Locate every Plasmodium vivax-infected red blood cell.
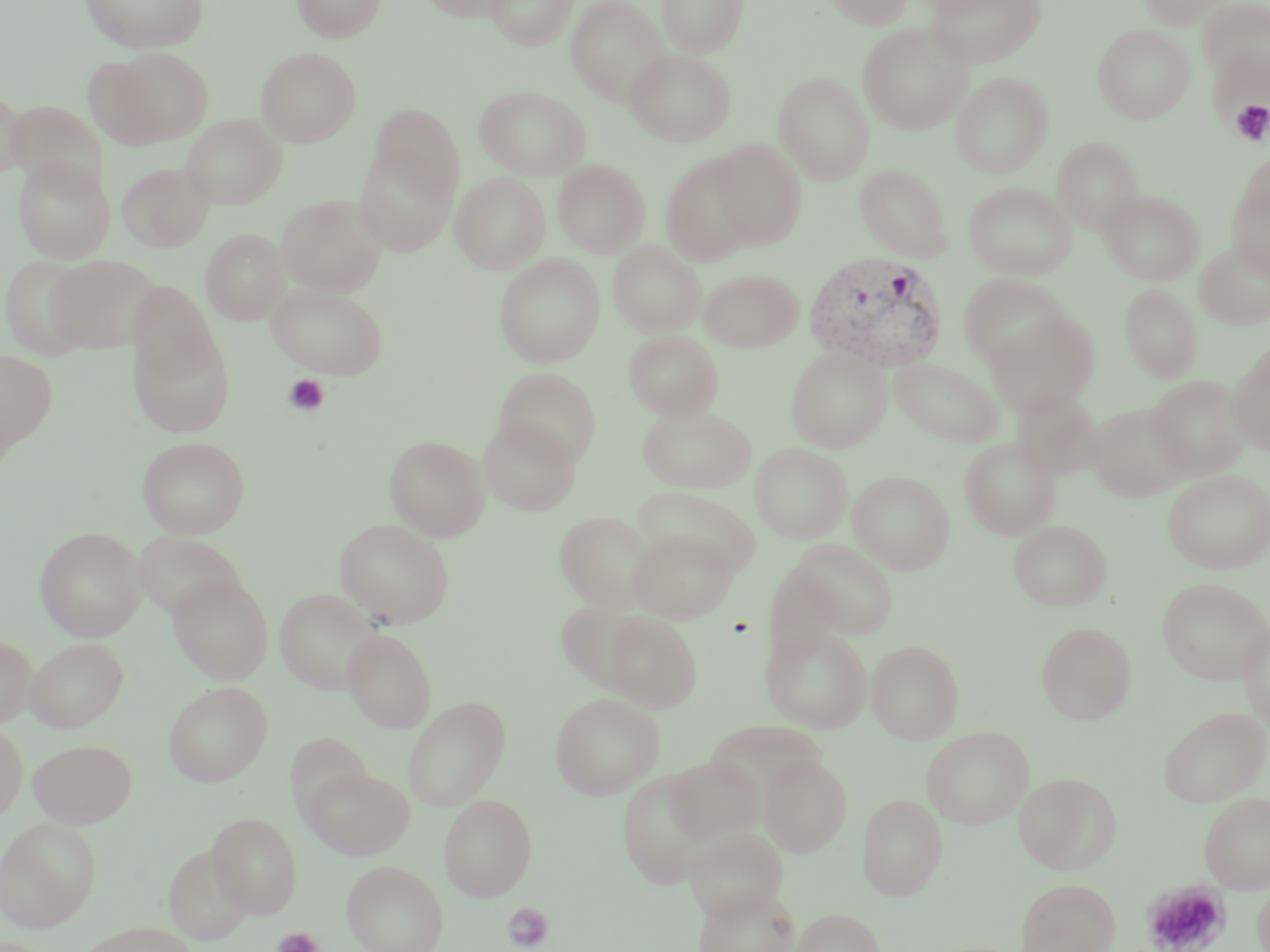

Approximate bounding boxes as (x1,y1)-(x2,y2) corner pairs in pixels.
Plasmodium vivax-infected red blood cells: (804,251)-(950,372).

Summary:
  - Platelet locations: (1230,101)-(1270,146), (283,374)-(330,417), (1144,881)-(1230,952), (503,902)-(555,951), (273,926)-(323,952)
  - Uninfected red blood cell locations: (79,0)-(208,53), (292,0)-(387,42), (420,0)-(518,22), (484,0)-(578,50), (566,0)-(671,106), (657,0)-(750,56), (822,0)-(913,28), (927,0)-(1046,68), (1139,0)-(1224,29), (1197,0)-(1270,84), (858,21)-(973,135), (1093,24)-(1195,123), (110,47)-(214,145), (256,47)-(361,147), (624,49)-(735,146), (951,71)-(1053,177), (773,73)-(874,184), (475,86)-(590,180), (0,87)-(28,178), (6,101)-(108,195), (370,103)-(464,202), (182,114)-(287,209), (1052,137)-(1144,234), (355,138)-(459,256), (711,138)-(808,250), (661,152)-(758,266), (1235,152)-(1270,241), (13,157)-(116,263), (553,159)-(649,258), (116,162)-(214,252), (855,164)-(952,260), (451,172)-(551,273), (1227,175)-(1270,281), (964,182)-(1076,279), (1100,190)-(1204,284), (277,195)-(387,296), (201,229)-(289,324), (1195,240)-(1270,329), (608,241)-(705,337), (1,254)-(94,360), (47,254)-(162,354), (494,254)-(605,367), (699,269)-(803,351), (958,273)-(1069,369), (128,281)-(221,388), (266,283)-(388,379), (1119,283)-(1203,383), (985,310)-(1100,417), (129,328)-(237,436), (624,331)-(723,420), (1229,345)-(1270,455), (786,346)-(891,451), (0,348)-(58,456), (890,357)-(1005,446), (495,367)-(602,467), (1148,375)-(1251,480), (1011,389)-(1103,480), (1086,403)-(1191,501), (637,405)-(756,493), (478,417)-(581,515), (385,435)-(490,541), (137,436)-(251,539), (960,437)-(1062,539), (749,443)-(853,544), (848,470)-(954,574), (1163,470)-(1270,574), (634,486)-(761,576), (555,511)-(658,611), (334,519)-(455,628), (1009,521)-(1111,610), (35,527)-(146,641), (628,529)-(736,623), (133,531)-(246,620), (790,540)-(897,639), (764,567)-(853,660), (168,572)-(273,684), (1156,577)-(1270,685), (275,588)-(382,695), (556,600)-(652,693), (602,611)-(702,711), (1238,619)-(1270,732), (1036,622)-(1136,724), (761,624)-(873,733), (343,629)-(437,732), (0,634)-(37,727), (26,637)-(129,732), (866,640)-(964,743), (163,682)-(273,786), (550,693)-(664,799), (403,696)-(510,811), (1158,706)-(1269,806), (706,721)-(828,803), (0,722)-(28,821), (922,726)-(1033,829), (285,732)-(374,821), (28,738)-(137,827), (666,756)-(764,843), (760,756)-(852,856), (302,766)-(415,860), (618,770)-(716,888), (1013,772)-(1121,874), (857,793)-(947,900), (1200,793)-(1270,893), (439,794)-(537,900), (208,811)-(302,918), (0,819)-(101,931), (684,827)-(788,923), (164,844)-(254,946), (342,860)-(448,952), (1017,878)-(1120,952), (1253,880)-(1270,952), (695,886)-(802,952), (791,908)-(885,952), (78,920)-(199,952)
  - Slide-level diagnosis: Plasmodium vivax
  - Modality: optical microscopy
  - Image size: 1270×952 pixels
  - Preparation: thin blood film
  - Stain: May-Grünwald-Giemsa
  - Field of view: single
  - Magnification: 1000x